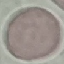 Malaria status: uninfected. Giemsa stain. Photographed with a smartphone camera at the microscope eyepiece. Automatically extracted cell patch, resized to 64 × 64 pixels. Thin blood smear.